Point out each leukocyte.
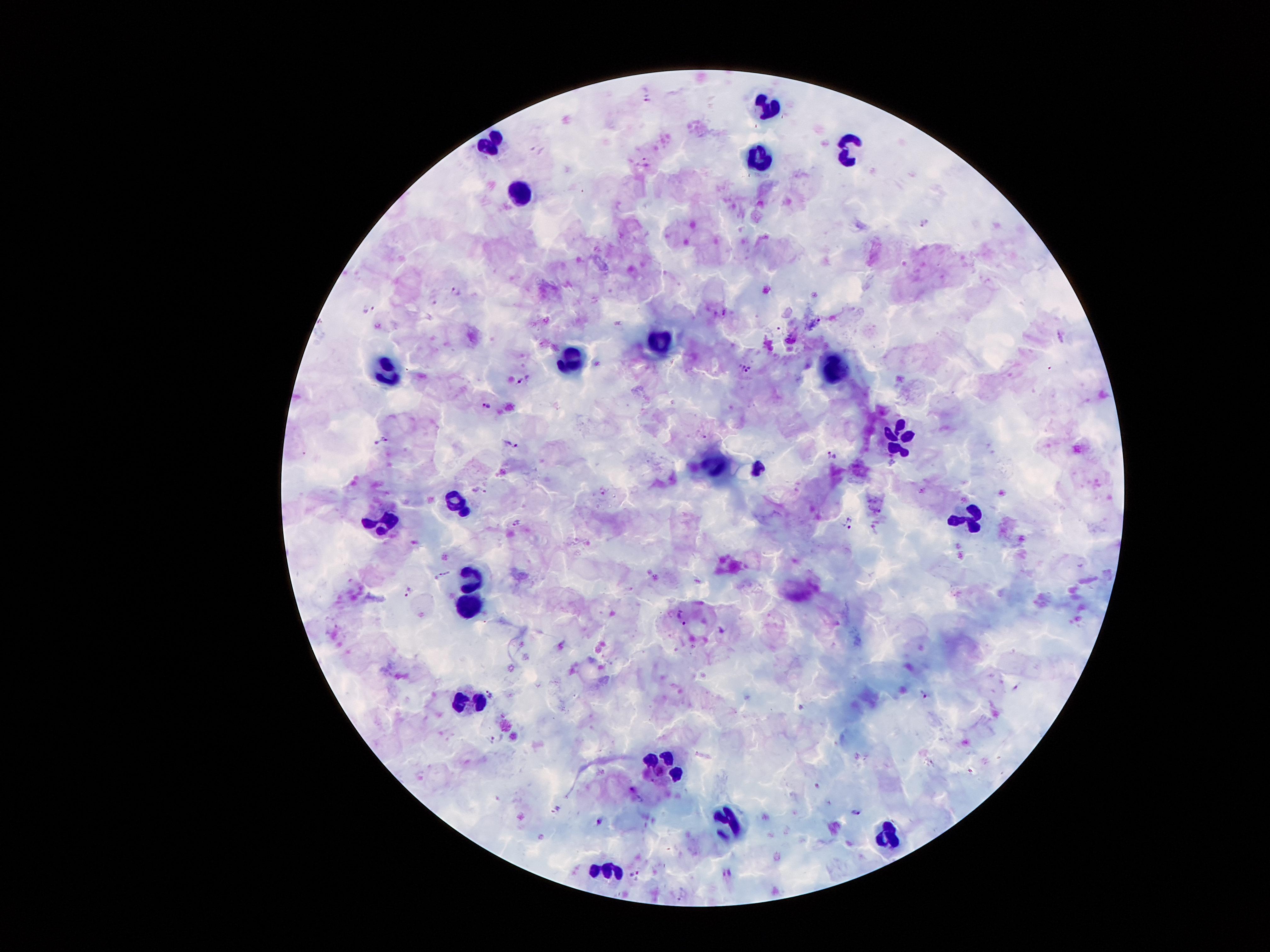

Approximate centers as (x, y) in pixels.
Leukocytes: (770, 107), (493, 142), (847, 152), (761, 158), (516, 189), (661, 343), (571, 363), (833, 367), (386, 369), (898, 438), (715, 464), (756, 468), (456, 497), (969, 521), (377, 523), (473, 571), (464, 604), (471, 701), (663, 764), (725, 817), (889, 834), (612, 869).

Summary:
  - Malaria parasite locations: (926, 223), (456, 292), (725, 311), (488, 405), (706, 438), (518, 522), (410, 592), (490, 695), (925, 695), (491, 740), (640, 800), (855, 813), (600, 821)
  - Preparation: thick blood smear
  - Image size: 1270×952 pixels
  - Stain: Giemsa
  - Patient malaria status: positive for Plasmodium falciparum
  - Field of view: one from this slide
  - Magnification: 100x
  - Capture: smartphone camera through the microscope eyepiece